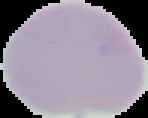
{
  "image_size": "148×118 pixels",
  "preparation": "thin blood film",
  "result": "negative for malaria parasites",
  "image_type": "cell region segmented out of the field of view; surrounding area masked to black"
}